Name the parasite shown.
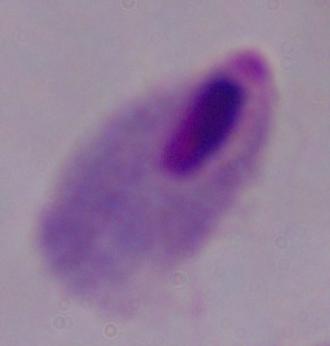

This is a trichomonad.

Summary:
  - Modality: photomicrograph
  - Magnification: 1000x